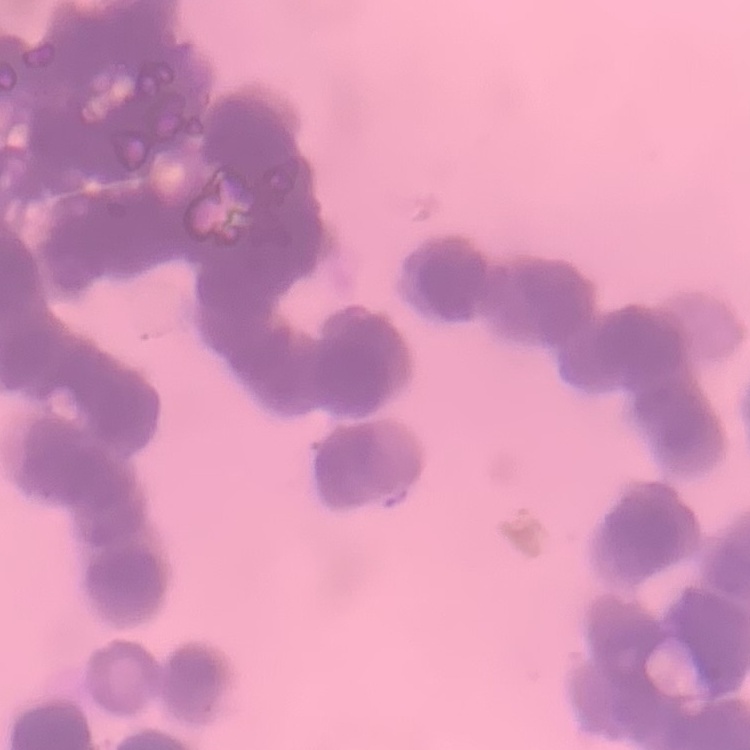

Summary:
  - Red blood cell morphology: rouleaux formation
  - Stain: Field's or Giemsa
  - Preparation: thin blood smear
  - Image type: one tile cut from a larger photomicrograph